Assess the morphology of the red blood cells.
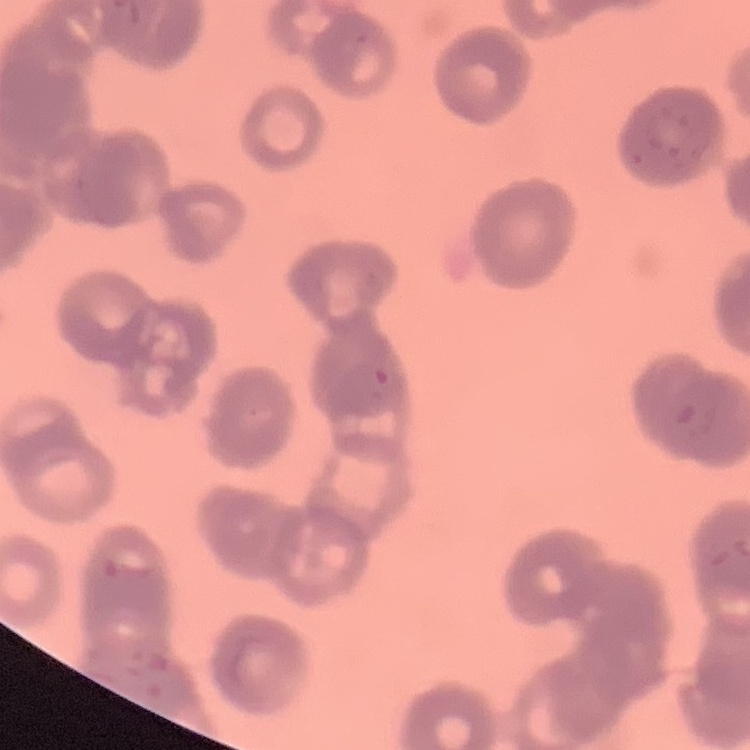
They show rouleaux formation.

Thin blood film. Field's or Giemsa stain. One tile cut from a larger photomicrograph.